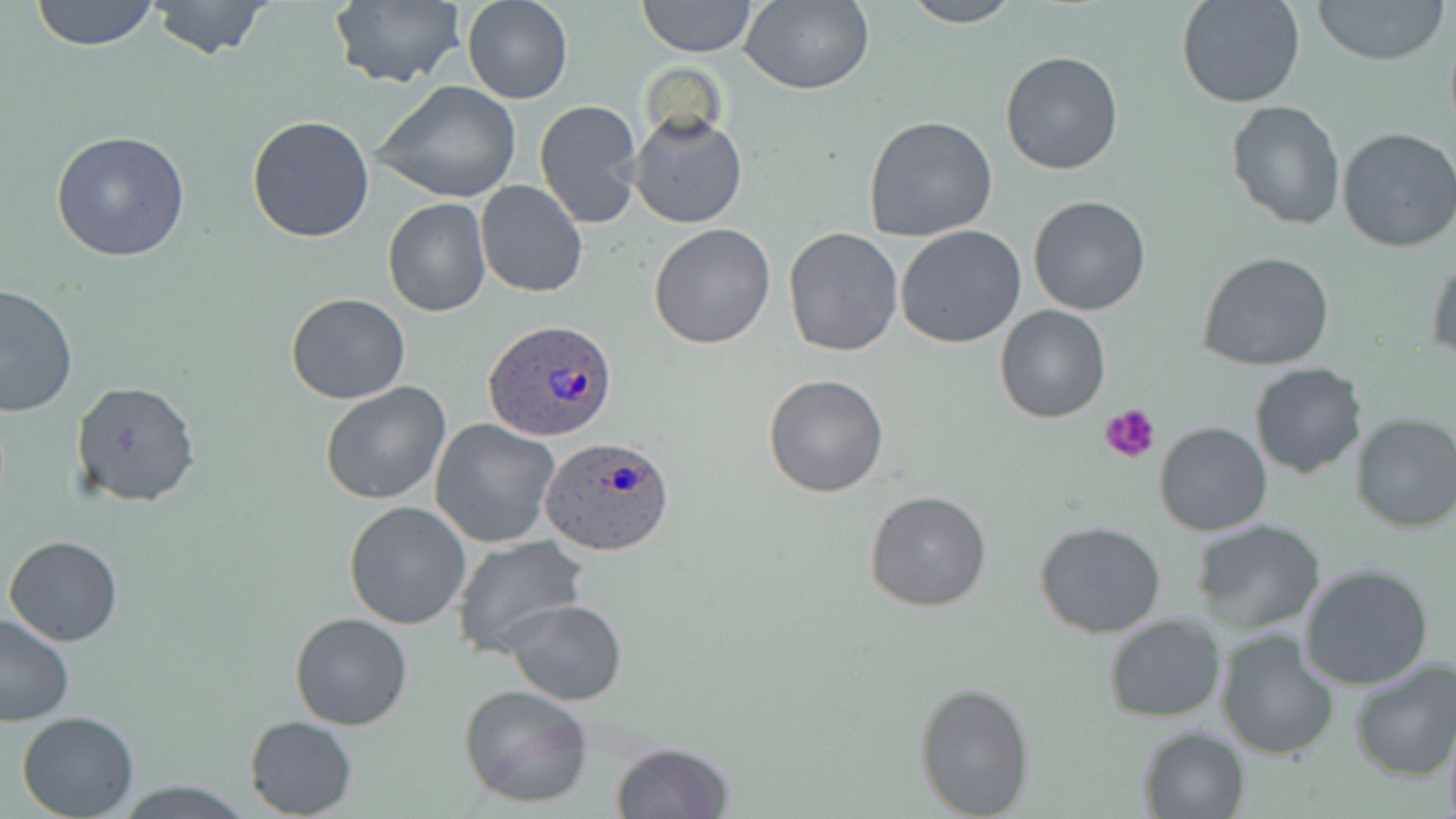

Summary:
  - Coordinate format: approximate bounding boxes as [x1, y1, x2, y2] in pixels
  - Uninfected red blood cell locations: [29, 0, 161, 51], [325, 0, 467, 90], [461, 0, 574, 104], [637, 0, 756, 57], [897, 0, 1021, 27], [1177, 0, 1307, 108], [1310, 0, 1449, 64], [147, 1, 274, 60], [739, 1, 874, 94], [1000, 50, 1125, 175], [374, 81, 522, 205], [534, 99, 644, 228], [1227, 99, 1344, 228], [629, 111, 747, 229], [246, 114, 377, 244], [864, 114, 998, 244], [1336, 128, 1456, 251], [51, 131, 192, 262], [476, 181, 586, 298], [1027, 196, 1152, 317], [382, 198, 491, 318], [648, 222, 778, 350], [896, 226, 1026, 350], [784, 227, 903, 356], [1427, 245, 1456, 361], [1197, 250, 1335, 372], [1, 283, 77, 417], [285, 292, 411, 405], [994, 304, 1110, 423], [1249, 364, 1366, 479], [763, 374, 890, 498], [70, 380, 200, 506], [318, 380, 452, 505], [1349, 413, 1456, 534], [431, 419, 561, 548], [1154, 421, 1272, 535], [864, 489, 993, 612], [344, 501, 473, 629], [1034, 521, 1167, 639], [1191, 521, 1326, 635], [5, 535, 123, 646], [449, 535, 590, 657], [1299, 562, 1434, 689], [504, 599, 628, 705], [0, 611, 75, 724], [289, 611, 414, 730], [1104, 615, 1226, 723], [1215, 628, 1342, 761], [1348, 660, 1456, 781], [913, 680, 1036, 818], [457, 683, 594, 808], [16, 712, 140, 819], [244, 714, 358, 817], [1138, 726, 1250, 818], [610, 742, 734, 819]
  - Plasmodium ovale-infected red blood cell locations: [485, 321, 619, 442], [540, 435, 676, 559]
  - Platelet locations: [1100, 403, 1159, 464]
  - Slide-level diagnosis: Plasmodium ovale
  - Stain: May-Grünwald-Giemsa
  - Magnification: 1000x
  - Field of view: single
  - Modality: light microscopy
  - Image size: 1456×819 pixels
  - Preparation: thin blood film